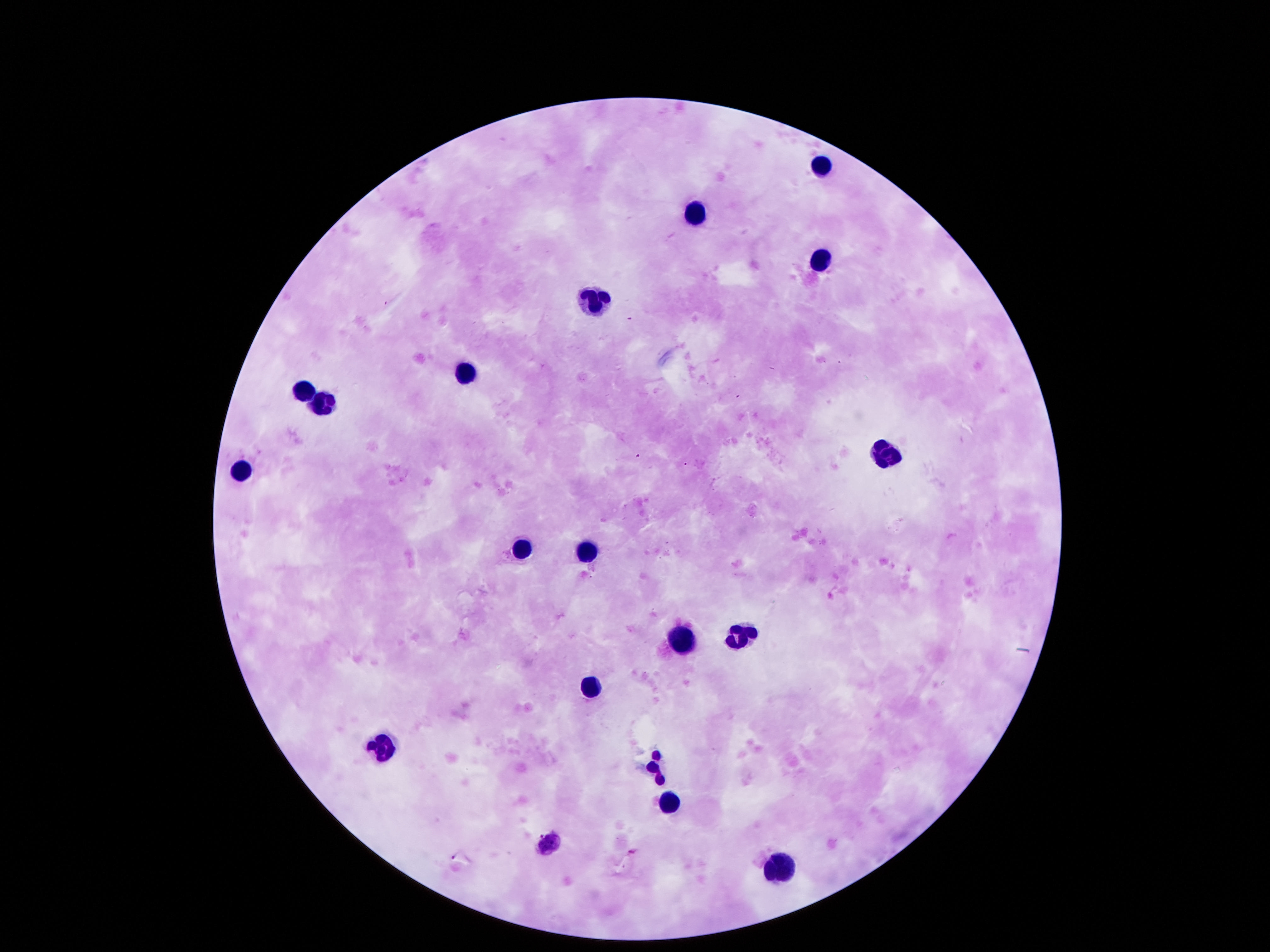

Approximate centers as {x, y} in pixels. Leukocyte locations: {824, 165}, {693, 212}, {817, 261}, {592, 298}, {464, 372}, {299, 393}, {319, 402}, {884, 456}, {242, 467}, {521, 548}, {585, 551}, {736, 632}, {676, 641}, {595, 685}, {380, 745}, {652, 765}, {669, 803}, {552, 842}, {777, 873}. 100x magnification. Photographed through the microscope eyepiece with a smartphone camera. Thick blood film. Patient malaria status: uninfected. Giemsa-stained preparation. One field from this slide. Image is 1270×952 pixels.